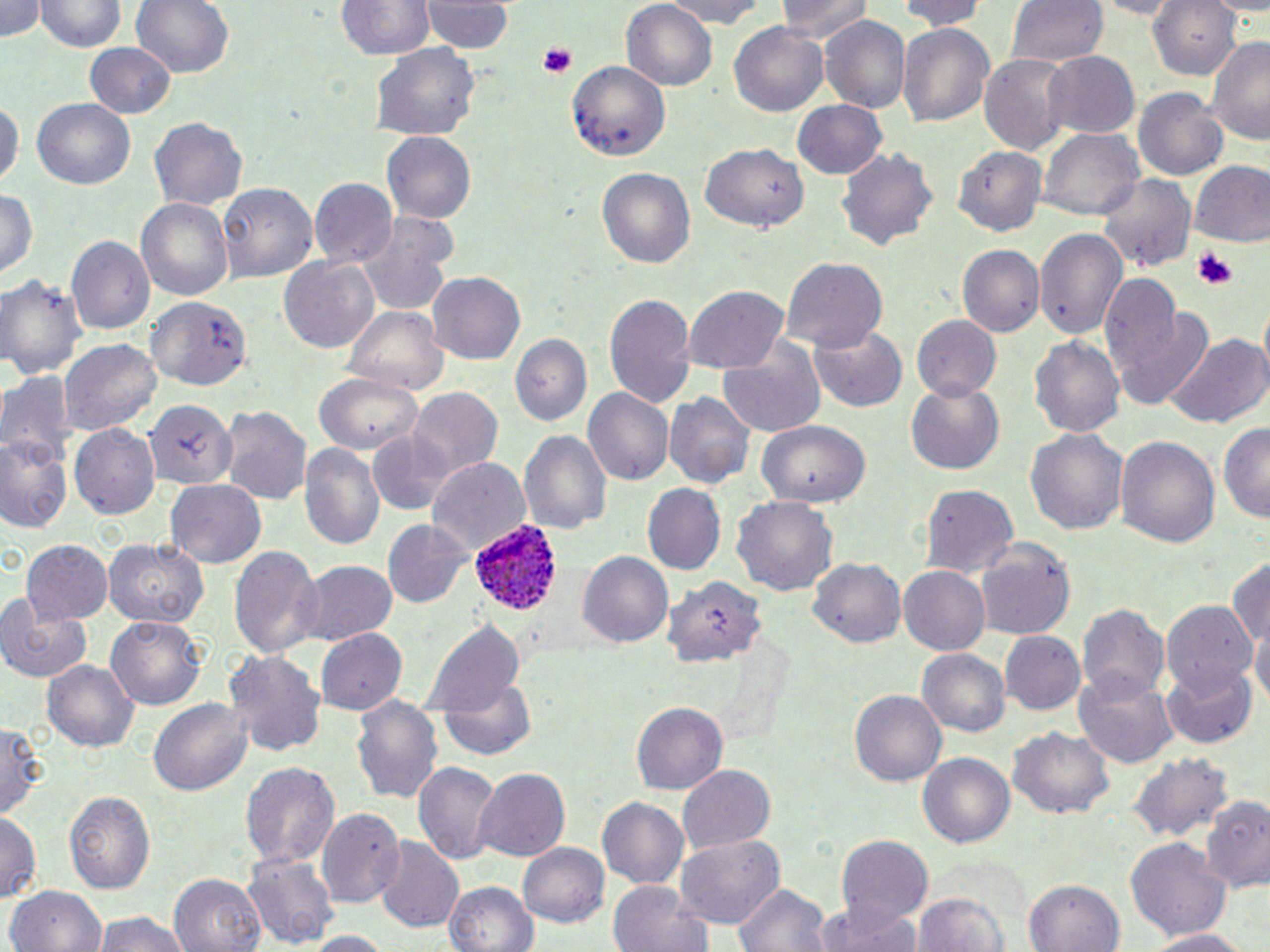
slide-level diagnosis = Plasmodium ovale
field of view = single
magnification = 1000x
Plasmodium ovale-infected red blood cell locations = approximate bounding boxes as named x1/y1/x2/y2 corners in pixels: (x1=470, y1=515, x2=562, y2=616)
uninfected red blood cell locations = approximate bounding boxes as named x1/y1/x2/y2 corners in pixels: (x1=0, y1=0, x2=50, y2=43), (x1=39, y1=0, x2=125, y2=55), (x1=130, y1=0, x2=233, y2=81), (x1=651, y1=0, x2=775, y2=26), (x1=775, y1=0, x2=872, y2=44), (x1=898, y1=0, x2=991, y2=30), (x1=1008, y1=0, x2=1108, y2=67), (x1=1082, y1=0, x2=1185, y2=18), (x1=335, y1=1, x2=434, y2=61), (x1=424, y1=1, x2=512, y2=56), (x1=622, y1=1, x2=718, y2=91), (x1=1150, y1=1, x2=1239, y2=81), (x1=820, y1=14, x2=911, y2=112), (x1=730, y1=20, x2=831, y2=118), (x1=897, y1=21, x2=996, y2=131), (x1=1205, y1=30, x2=1270, y2=144), (x1=85, y1=43, x2=173, y2=119), (x1=373, y1=43, x2=480, y2=144), (x1=980, y1=50, x2=1074, y2=158), (x1=1042, y1=51, x2=1139, y2=140), (x1=566, y1=59, x2=671, y2=156), (x1=1134, y1=88, x2=1229, y2=184), (x1=0, y1=93, x2=21, y2=190), (x1=33, y1=100, x2=136, y2=188), (x1=792, y1=100, x2=888, y2=179), (x1=149, y1=115, x2=248, y2=210), (x1=1040, y1=130, x2=1143, y2=219), (x1=383, y1=132, x2=477, y2=224), (x1=701, y1=143, x2=808, y2=233), (x1=956, y1=143, x2=1048, y2=237), (x1=835, y1=146, x2=939, y2=253), (x1=1189, y1=161, x2=1270, y2=248), (x1=596, y1=167, x2=694, y2=271), (x1=1099, y1=173, x2=1194, y2=274), (x1=309, y1=178, x2=398, y2=269), (x1=217, y1=183, x2=318, y2=283), (x1=0, y1=187, x2=37, y2=281), (x1=135, y1=197, x2=232, y2=304), (x1=357, y1=215, x2=456, y2=317), (x1=1035, y1=227, x2=1126, y2=341), (x1=67, y1=236, x2=156, y2=335), (x1=958, y1=244, x2=1044, y2=339), (x1=781, y1=255, x2=889, y2=353), (x1=280, y1=256, x2=378, y2=353), (x1=426, y1=271, x2=527, y2=364), (x1=0, y1=273, x2=87, y2=384), (x1=1098, y1=274, x2=1183, y2=385), (x1=683, y1=287, x2=787, y2=375), (x1=604, y1=291, x2=694, y2=409), (x1=147, y1=296, x2=250, y2=389), (x1=1113, y1=301, x2=1216, y2=410), (x1=343, y1=304, x2=447, y2=396), (x1=912, y1=316, x2=1003, y2=402), (x1=810, y1=324, x2=908, y2=412), (x1=1030, y1=332, x2=1127, y2=441), (x1=509, y1=333, x2=591, y2=425), (x1=1164, y1=333, x2=1267, y2=430), (x1=59, y1=339, x2=162, y2=434), (x1=716, y1=345, x2=825, y2=438), (x1=0, y1=371, x2=75, y2=461), (x1=316, y1=373, x2=426, y2=453), (x1=906, y1=382, x2=1005, y2=475), (x1=407, y1=389, x2=502, y2=484), (x1=582, y1=390, x2=673, y2=488), (x1=665, y1=391, x2=753, y2=489), (x1=143, y1=397, x2=234, y2=490), (x1=220, y1=405, x2=311, y2=507), (x1=757, y1=422, x2=870, y2=505), (x1=1217, y1=422, x2=1270, y2=525), (x1=70, y1=424, x2=161, y2=520), (x1=1024, y1=425, x2=1128, y2=539), (x1=519, y1=428, x2=612, y2=540), (x1=2, y1=431, x2=76, y2=536), (x1=367, y1=431, x2=452, y2=516), (x1=1117, y1=435, x2=1219, y2=546), (x1=297, y1=443, x2=386, y2=552), (x1=427, y1=458, x2=530, y2=557), (x1=166, y1=478, x2=265, y2=565), (x1=918, y1=484, x2=1018, y2=578), (x1=645, y1=485, x2=726, y2=575), (x1=732, y1=497, x2=837, y2=599), (x1=381, y1=518, x2=471, y2=610), (x1=100, y1=535, x2=208, y2=631), (x1=21, y1=540, x2=114, y2=626), (x1=975, y1=540, x2=1078, y2=639), (x1=229, y1=542, x2=322, y2=658), (x1=578, y1=551, x2=673, y2=650), (x1=1229, y1=553, x2=1270, y2=660), (x1=808, y1=555, x2=908, y2=648), (x1=294, y1=560, x2=396, y2=646), (x1=898, y1=566, x2=990, y2=656), (x1=659, y1=572, x2=771, y2=669), (x1=1202, y1=578, x2=1267, y2=692), (x1=0, y1=594, x2=91, y2=682), (x1=1077, y1=602, x2=1168, y2=703), (x1=1163, y1=603, x2=1255, y2=694), (x1=104, y1=614, x2=204, y2=711), (x1=1250, y1=615, x2=1270, y2=715), (x1=423, y1=618, x2=526, y2=719), (x1=316, y1=629, x2=407, y2=713), (x1=999, y1=631, x2=1085, y2=716), (x1=916, y1=649, x2=1009, y2=737), (x1=226, y1=650, x2=326, y2=759), (x1=42, y1=659, x2=139, y2=754), (x1=1163, y1=664, x2=1258, y2=748), (x1=1076, y1=666, x2=1179, y2=770), (x1=440, y1=674, x2=537, y2=761), (x1=850, y1=690, x2=946, y2=789), (x1=351, y1=697, x2=443, y2=802), (x1=147, y1=698, x2=253, y2=796), (x1=629, y1=699, x2=729, y2=793), (x1=0, y1=721, x2=47, y2=817), (x1=1009, y1=726, x2=1113, y2=822), (x1=1126, y1=750, x2=1233, y2=845), (x1=919, y1=753, x2=1016, y2=851), (x1=239, y1=760, x2=340, y2=869), (x1=414, y1=761, x2=502, y2=867), (x1=676, y1=763, x2=776, y2=854), (x1=473, y1=767, x2=572, y2=862), (x1=64, y1=792, x2=155, y2=892), (x1=1202, y1=794, x2=1270, y2=895), (x1=598, y1=797, x2=689, y2=888), (x1=316, y1=807, x2=405, y2=909), (x1=0, y1=810, x2=41, y2=904), (x1=675, y1=834, x2=784, y2=928), (x1=834, y1=836, x2=933, y2=928), (x1=376, y1=837, x2=465, y2=934), (x1=1126, y1=838, x2=1231, y2=941), (x1=517, y1=842, x2=609, y2=929), (x1=243, y1=853, x2=339, y2=951), (x1=169, y1=873, x2=267, y2=952), (x1=607, y1=878, x2=706, y2=952), (x1=1024, y1=878, x2=1127, y2=952), (x1=443, y1=881, x2=541, y2=952), (x1=732, y1=882, x2=832, y2=952), (x1=6, y1=885, x2=106, y2=952), (x1=913, y1=889, x2=1014, y2=952), (x1=817, y1=900, x2=923, y2=952), (x1=85, y1=912, x2=191, y2=952), (x1=1144, y1=928, x2=1253, y2=951), (x1=294, y1=931, x2=395, y2=952)
stain = May-Grünwald-Giemsa
modality = light microscopy
platelet locations = approximate bounding boxes as named x1/y1/x2/y2 corners in pixels: (x1=539, y1=44, x2=576, y2=79), (x1=1193, y1=248, x2=1234, y2=287)
preparation = thin blood smear
image size = 1270×952 pixels